Identify the parasite.
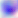
This is Toxoplasma gondii.

Photomicrograph. Captured at 400x magnification.